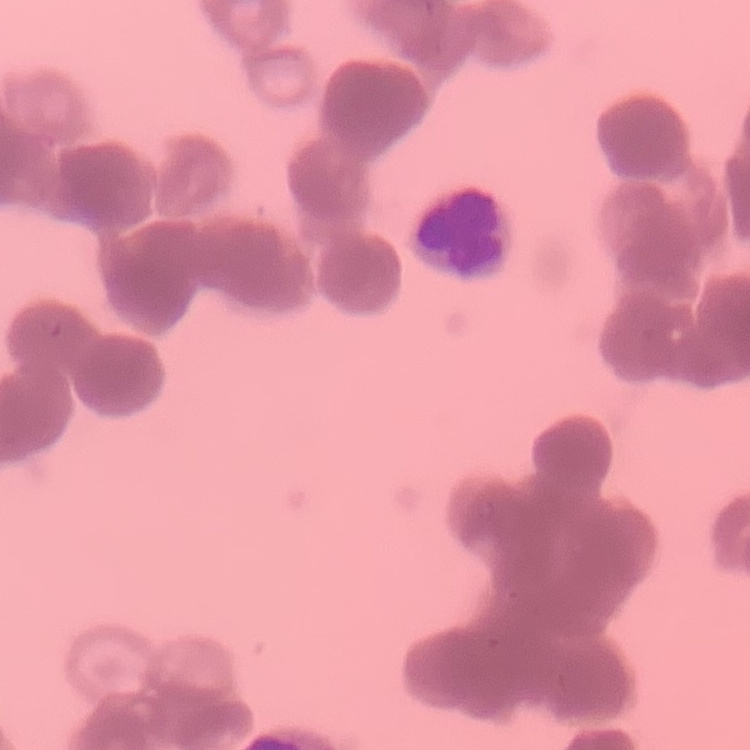
{
  "red_blood_cell_morphology": "rouleaux formation",
  "image_type": "square crop of a larger photomicrograph",
  "preparation": "thin blood film",
  "stain": "Field's or Giemsa"
}